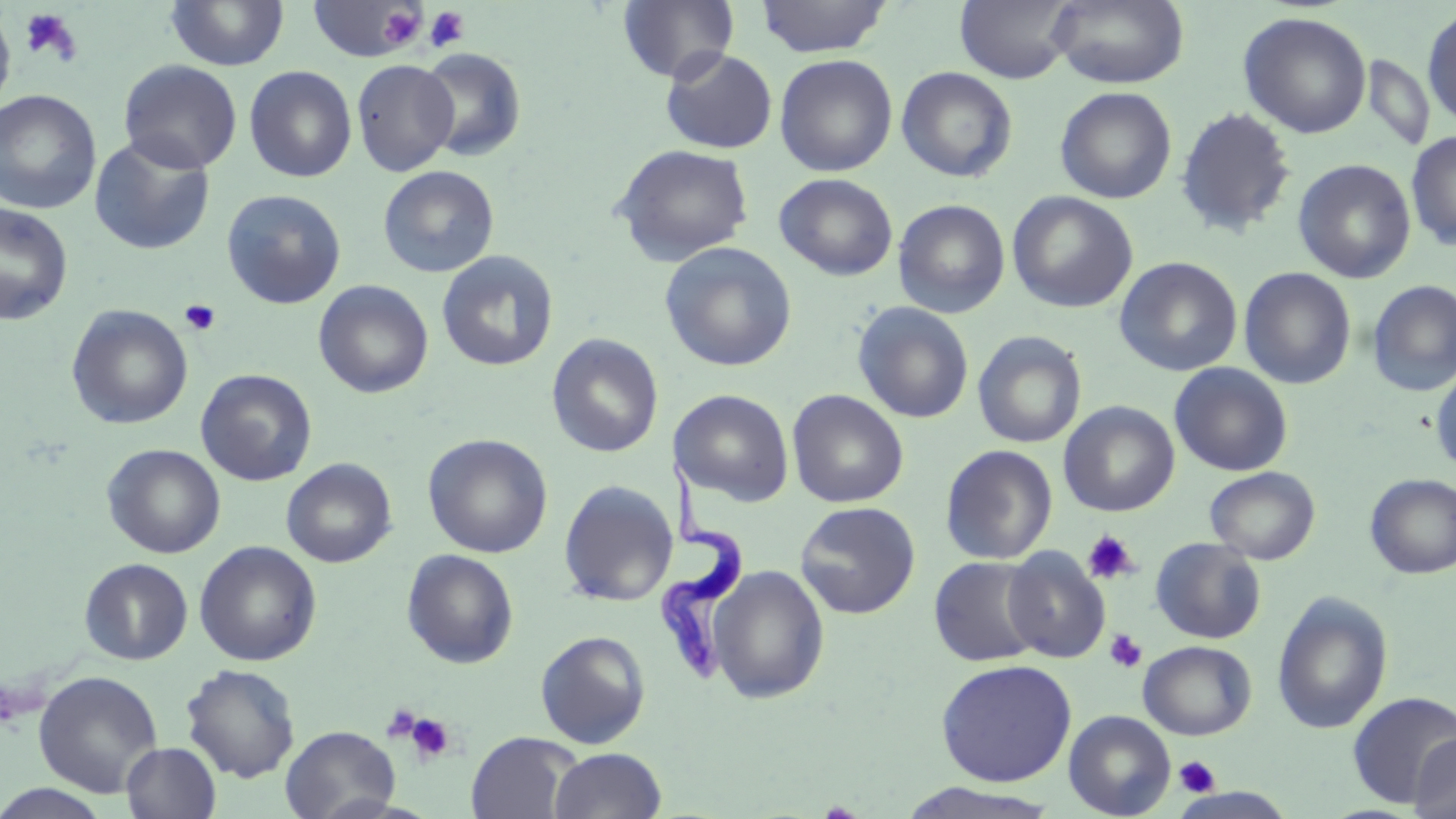
Summary:
  - Coordinate format: approximate bounding boxes as named x1/y1/x2/y2 corners in pixels
  - Uninfected red blood cell locations: (x1=165, y1=0, x2=290, y2=72), (x1=755, y1=0, x2=892, y2=58), (x1=955, y1=0, x2=1078, y2=84), (x1=1049, y1=0, x2=1189, y2=89), (x1=308, y1=1, x2=423, y2=62), (x1=617, y1=1, x2=739, y2=84), (x1=0, y1=6, x2=16, y2=115), (x1=1422, y1=7, x2=1456, y2=128), (x1=1238, y1=11, x2=1372, y2=139), (x1=416, y1=47, x2=526, y2=162), (x1=661, y1=48, x2=778, y2=154), (x1=774, y1=54, x2=897, y2=177), (x1=1360, y1=55, x2=1434, y2=152), (x1=118, y1=59, x2=242, y2=174), (x1=351, y1=59, x2=459, y2=176), (x1=244, y1=65, x2=357, y2=182), (x1=897, y1=66, x2=1018, y2=183), (x1=1055, y1=86, x2=1177, y2=204), (x1=0, y1=89, x2=102, y2=214), (x1=1175, y1=106, x2=1296, y2=238), (x1=1406, y1=131, x2=1456, y2=251), (x1=89, y1=134, x2=215, y2=256), (x1=612, y1=144, x2=754, y2=266), (x1=1293, y1=159, x2=1416, y2=283), (x1=378, y1=165, x2=500, y2=278), (x1=774, y1=173, x2=898, y2=280), (x1=222, y1=189, x2=346, y2=309), (x1=1007, y1=191, x2=1138, y2=313), (x1=893, y1=199, x2=1010, y2=318), (x1=0, y1=203, x2=73, y2=325), (x1=658, y1=241, x2=797, y2=372), (x1=436, y1=250, x2=559, y2=372), (x1=1114, y1=256, x2=1243, y2=376), (x1=1239, y1=267, x2=1356, y2=389), (x1=1367, y1=279, x2=1456, y2=396), (x1=314, y1=280, x2=434, y2=399), (x1=852, y1=301, x2=974, y2=424), (x1=66, y1=305, x2=193, y2=430), (x1=972, y1=330, x2=1087, y2=449), (x1=547, y1=334, x2=664, y2=458), (x1=1169, y1=362, x2=1293, y2=476), (x1=1430, y1=367, x2=1456, y2=475), (x1=196, y1=369, x2=317, y2=486), (x1=672, y1=389, x2=794, y2=506), (x1=787, y1=389, x2=908, y2=508), (x1=1059, y1=401, x2=1180, y2=517), (x1=422, y1=433, x2=553, y2=558), (x1=102, y1=444, x2=225, y2=558), (x1=940, y1=444, x2=1058, y2=564), (x1=282, y1=458, x2=397, y2=568), (x1=1204, y1=466, x2=1320, y2=564), (x1=1365, y1=473, x2=1456, y2=579), (x1=558, y1=479, x2=679, y2=607), (x1=794, y1=501, x2=921, y2=619), (x1=1151, y1=538, x2=1266, y2=644), (x1=194, y1=540, x2=322, y2=666), (x1=1002, y1=547, x2=1111, y2=663), (x1=402, y1=549, x2=519, y2=668), (x1=929, y1=556, x2=1044, y2=667), (x1=79, y1=558, x2=193, y2=665), (x1=708, y1=565, x2=830, y2=704), (x1=1272, y1=591, x2=1392, y2=734), (x1=535, y1=630, x2=651, y2=748), (x1=1138, y1=640, x2=1256, y2=740), (x1=935, y1=659, x2=1077, y2=787), (x1=181, y1=663, x2=300, y2=783), (x1=33, y1=670, x2=163, y2=798), (x1=1348, y1=690, x2=1456, y2=808), (x1=1063, y1=710, x2=1176, y2=819), (x1=281, y1=725, x2=400, y2=819), (x1=466, y1=731, x2=580, y2=819), (x1=1409, y1=733, x2=1456, y2=819), (x1=121, y1=742, x2=221, y2=819), (x1=549, y1=748, x2=667, y2=819), (x1=898, y1=783, x2=1061, y2=819), (x1=0, y1=784, x2=114, y2=819)
  - Trypanosoma brucei locations: (x1=651, y1=448, x2=749, y2=694)
  - Platelet locations: (x1=320, y1=0, x2=428, y2=59), (x1=378, y1=5, x2=425, y2=50), (x1=424, y1=6, x2=470, y2=52), (x1=19, y1=8, x2=83, y2=65), (x1=180, y1=299, x2=221, y2=335), (x1=1082, y1=530, x2=1139, y2=585), (x1=1104, y1=629, x2=1147, y2=673), (x1=380, y1=704, x2=422, y2=743), (x1=404, y1=712, x2=456, y2=764), (x1=1175, y1=755, x2=1220, y2=797)
  - Slide-level diagnosis: Trypanosoma brucei
  - Stain: May-Grünwald-Giemsa
  - Preparation: thin blood film
  - Modality: optical microscopy
  - Field of view: single
  - Magnification: 1000x
  - Image size: 1456×819 pixels